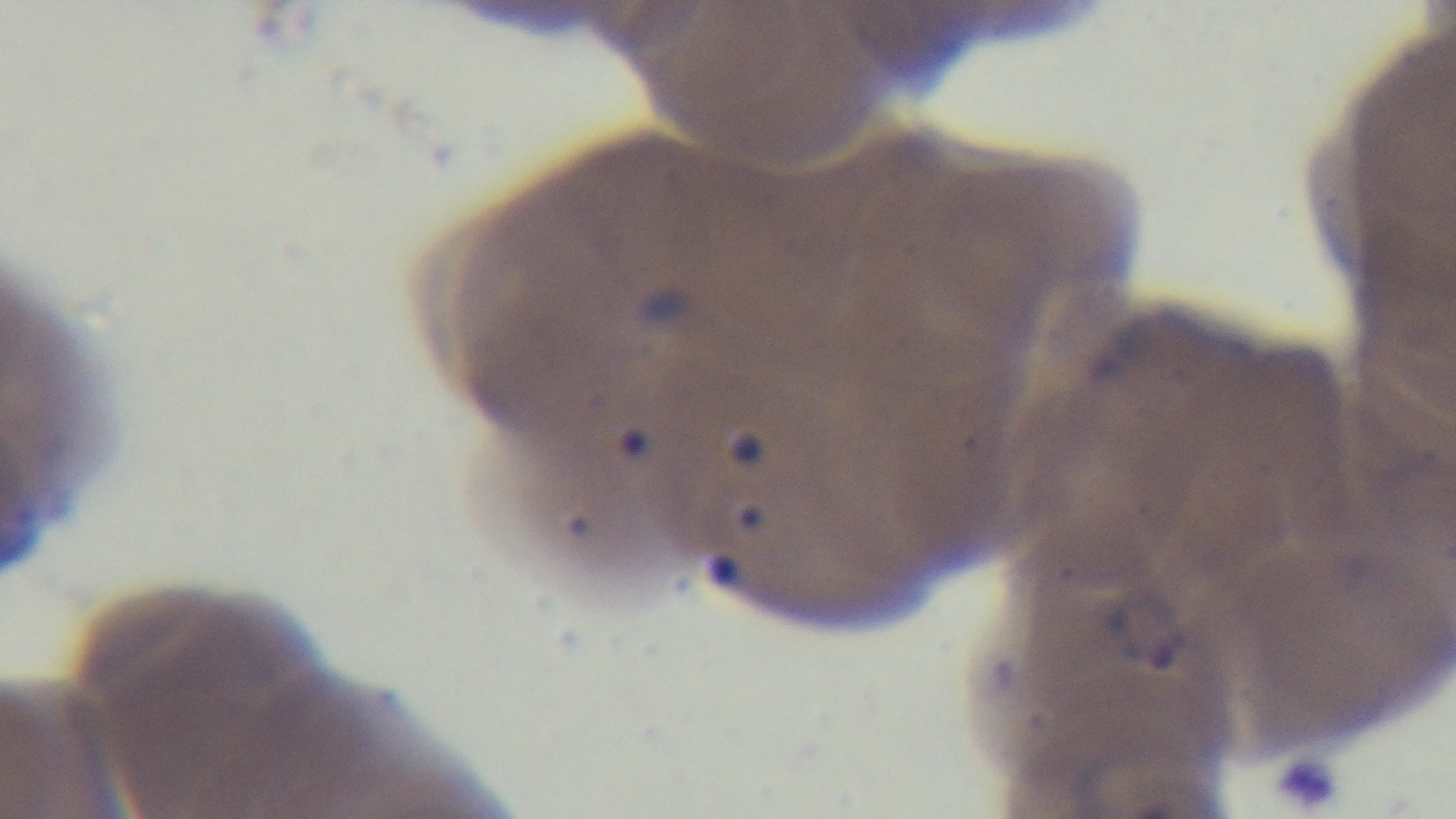
Summary:
  - Capture: mounted 4K digital camera
  - Objective: 100x oil immersion
  - Modality: light microscopy
  - Malaria status: infected
  - Preparation: thin blood film
  - Stain: Giemsa
  - Field of view: single